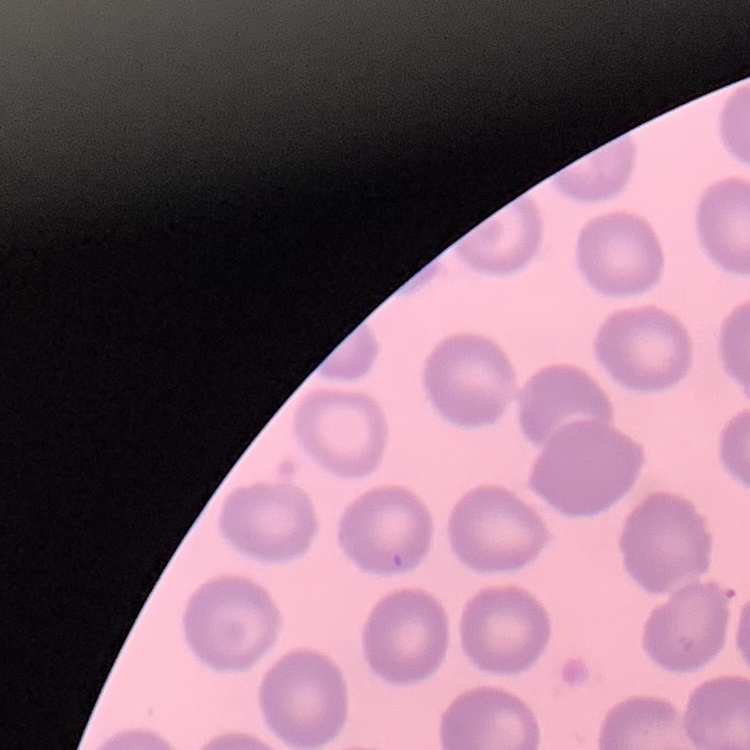 The red blood cells exhibit no rouleaux formation. Thin blood smear. Field's or Giemsa stain. One tile cut from a larger photomicrograph.